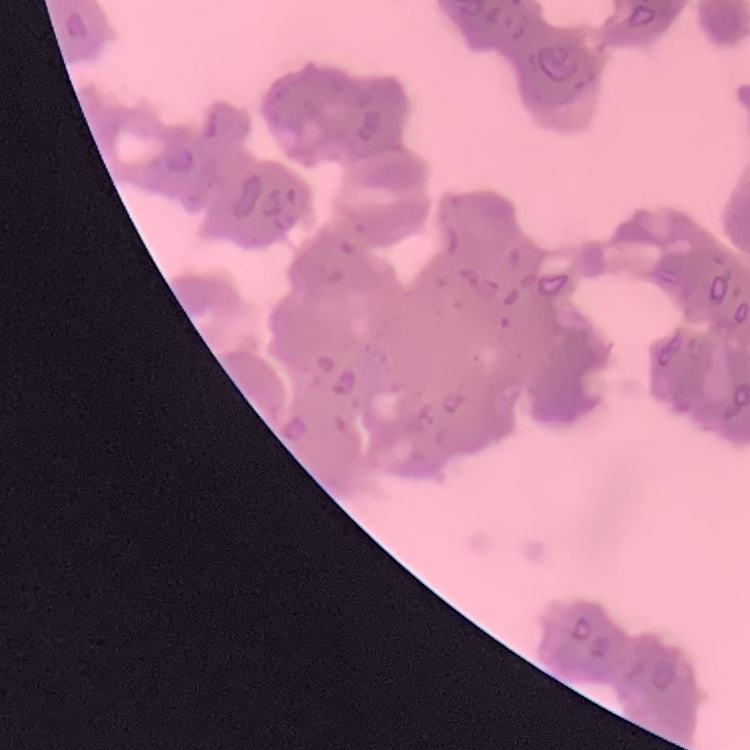
Summary:
  - Red blood cell morphology: rouleaux formation
  - Stain: Field's or Giemsa
  - Preparation: thin peripheral smear
  - Image type: square crop of a larger photomicrograph